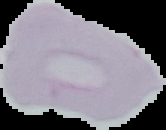
Malaria status: uninfected. Cell region segmented out of the field of view; the surrounding area is masked to black. Image is 166×130 pixels. From a thin blood film.